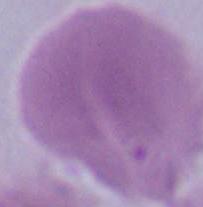

A red blood cell is seen. Micrograph. Captured at 1000x magnification.